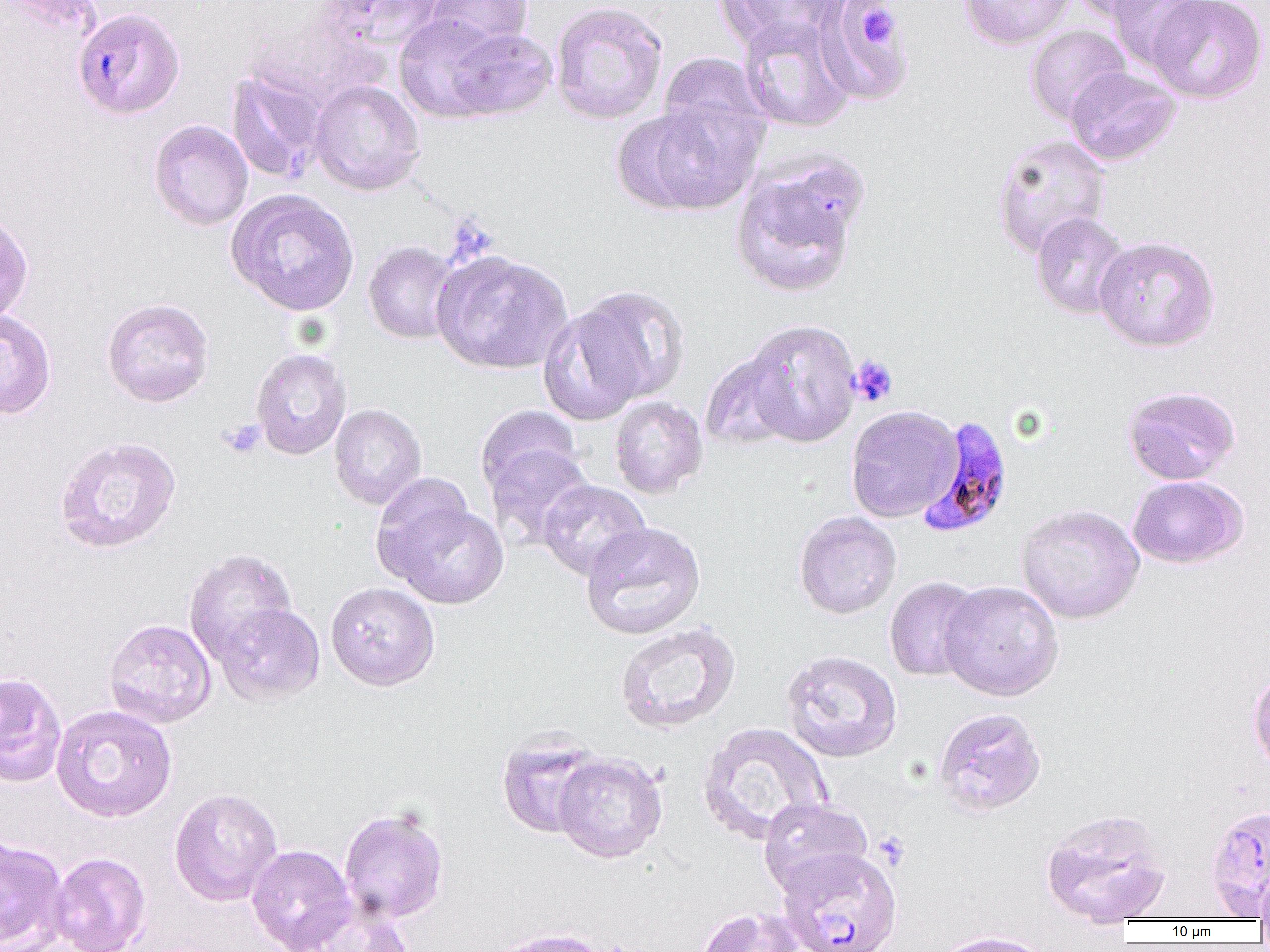

{
  "slide_level_diagnosis": "Plasmodium falciparum",
  "magnification": "1000x",
  "uninfected_red_blood_cell_locations": "approximate bounding boxes as [x1, y1, x2, y2] in pixels: [3, 0, 102, 34], [321, 0, 444, 54], [421, 0, 534, 56], [719, 0, 843, 51], [814, 0, 914, 106], [958, 0, 1075, 50], [1068, 0, 1172, 22], [1104, 0, 1214, 71], [1146, 0, 1268, 103], [549, 1, 669, 124], [394, 13, 510, 123], [738, 16, 857, 133], [1026, 24, 1131, 125], [443, 25, 559, 120], [657, 51, 770, 154], [1064, 67, 1181, 166], [226, 68, 330, 184], [309, 80, 425, 196], [632, 100, 767, 213], [149, 119, 253, 231], [991, 134, 1112, 259], [730, 162, 863, 299], [226, 188, 359, 316], [0, 210, 33, 325], [1030, 212, 1132, 320], [1093, 235, 1221, 352], [363, 241, 463, 344], [431, 250, 573, 375], [573, 285, 691, 402], [102, 298, 215, 407], [538, 305, 648, 426], [0, 308, 56, 419], [741, 318, 861, 447], [251, 348, 352, 460], [700, 351, 798, 451], [1121, 385, 1241, 485], [609, 396, 708, 498], [329, 404, 427, 510], [477, 404, 585, 502], [845, 405, 962, 522], [54, 436, 181, 554], [484, 443, 594, 549], [1128, 475, 1248, 569], [537, 479, 650, 580], [381, 496, 509, 608], [1016, 504, 1145, 624], [794, 511, 902, 619], [580, 521, 706, 640], [183, 548, 298, 665], [884, 577, 984, 682], [938, 579, 1064, 701], [326, 581, 440, 691], [215, 603, 326, 705], [104, 618, 217, 729], [613, 622, 741, 734], [781, 650, 903, 762], [1248, 668, 1270, 775], [0, 672, 67, 787], [51, 704, 177, 822], [933, 707, 1047, 816], [698, 721, 832, 845], [496, 732, 605, 838], [552, 752, 667, 863], [169, 787, 283, 906], [758, 797, 873, 898], [1205, 804, 1270, 917], [339, 807, 448, 924], [1040, 807, 1172, 925], [0, 836, 69, 952], [246, 845, 355, 952], [48, 851, 151, 952], [1255, 862, 1270, 928], [288, 897, 415, 952], [694, 906, 806, 952], [488, 927, 615, 952], [930, 930, 1055, 952]",
  "plasmodium_falciparum_infected_red_blood_cell_locations": "approximate bounding boxes as [x1, y1, x2, y2] in pixels: [73, 7, 185, 119], [917, 415, 1015, 537], [777, 848, 904, 952]",
  "modality": "optical microscopy",
  "field_of_view": "one of a larger specimen",
  "platelet_locations": "approximate bounding boxes as [x1, y1, x2, y2] in pixels: [859, 6, 898, 47], [849, 355, 899, 407], [220, 419, 266, 458], [873, 831, 911, 870]",
  "image_size": "1270×952 pixels",
  "preparation": "thin blood smear"
}